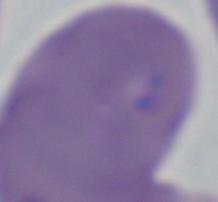

modality = micrograph
identification = Babesia
magnification = 1000x